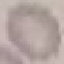

Malaria status: uninfected. Thin smear of blood. Automatically extracted cell patch, resized to 64 × 64 pixels. Giemsa stain. Acquired by smartphone through the microscope eyepiece.